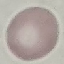
Summary:
  - Result: negative for malaria parasites
  - Preparation: thin smear
  - Capture: smartphone camera at the microscope eyepiece
  - Image type: automatically extracted cell patch, resized to 64 × 64 pixels
  - Stain: Giemsa